Locate and identify every blood parasite.
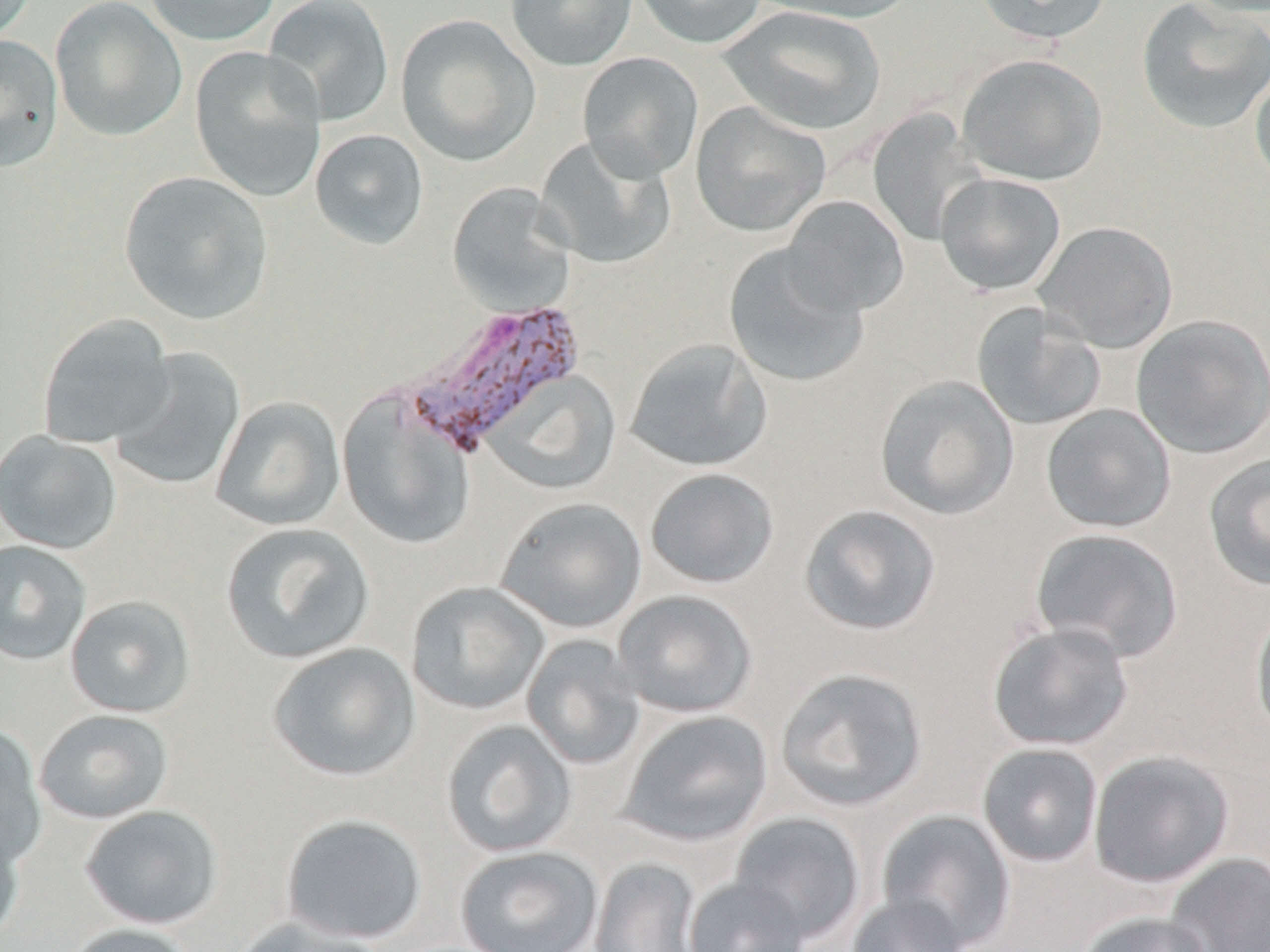

Approximate bounding boxes as (x1,y1)-(x2,y2) corner pairs in pixels.
Plasmodium vivax-infected red blood cells: (398,300)-(586,457).
No Plasmodium falciparum, Plasmodium ovale, Plasmodium malariae, Babesia divergens, or Trypanosoma brucei observed.

Summary:
  - Uninfected red blood cell locations: (0,0)-(37,44), (50,0)-(188,143), (142,0)-(283,46), (262,0)-(395,127), (505,0)-(638,72), (633,0)-(767,49), (751,0)-(919,24), (973,0)-(1113,45), (1136,0)-(1270,134), (719,6)-(887,135), (395,14)-(541,167), (0,34)-(63,171), (190,45)-(326,203), (577,52)-(704,183), (956,53)-(1107,186), (1249,66)-(1270,191), (690,101)-(831,237), (866,110)-(988,248), (310,129)-(429,250), (534,135)-(676,270), (119,171)-(273,324), (935,172)-(1066,295), (446,182)-(576,316), (781,195)-(910,317), (1034,221)-(1178,353), (722,243)-(870,388), (971,302)-(1107,431), (36,313)-(177,449), (1130,314)-(1270,458), (623,338)-(773,473), (107,348)-(245,493), (483,370)-(622,496), (874,374)-(1020,520), (337,389)-(477,551), (210,396)-(346,531), (1041,404)-(1176,533), (0,430)-(122,555), (1203,453)-(1270,590), (644,467)-(779,589), (495,496)-(647,634), (798,503)-(942,636), (220,522)-(375,664), (1029,528)-(1184,662), (0,540)-(92,665), (405,581)-(550,715), (613,589)-(758,718), (64,595)-(196,718), (1250,605)-(1270,740), (987,621)-(1133,752), (521,634)-(646,770), (267,642)-(421,782), (775,667)-(929,812), (33,709)-(174,824), (617,709)-(773,848), (440,719)-(577,858), (0,722)-(48,867), (976,743)-(1103,868), (1088,749)-(1235,888), (79,804)-(224,930), (876,809)-(1017,949), (729,812)-(865,945), (279,813)-(428,944), (0,815)-(25,944), (454,846)-(603,951), (1164,853)-(1270,952), (589,857)-(703,952), (682,876)-(810,952), (846,893)-(970,952), (1074,911)-(1214,952), (230,917)-(387,952), (60,923)-(198,952)
  - Slide-level diagnosis: Plasmodium vivax
  - Stain: May-Grünwald-Giemsa
  - Preparation: thin blood smear
  - Modality: optical microscopy
  - Magnification: 1000x
  - Image size: 1270×952 pixels
  - Field of view: one of a larger specimen